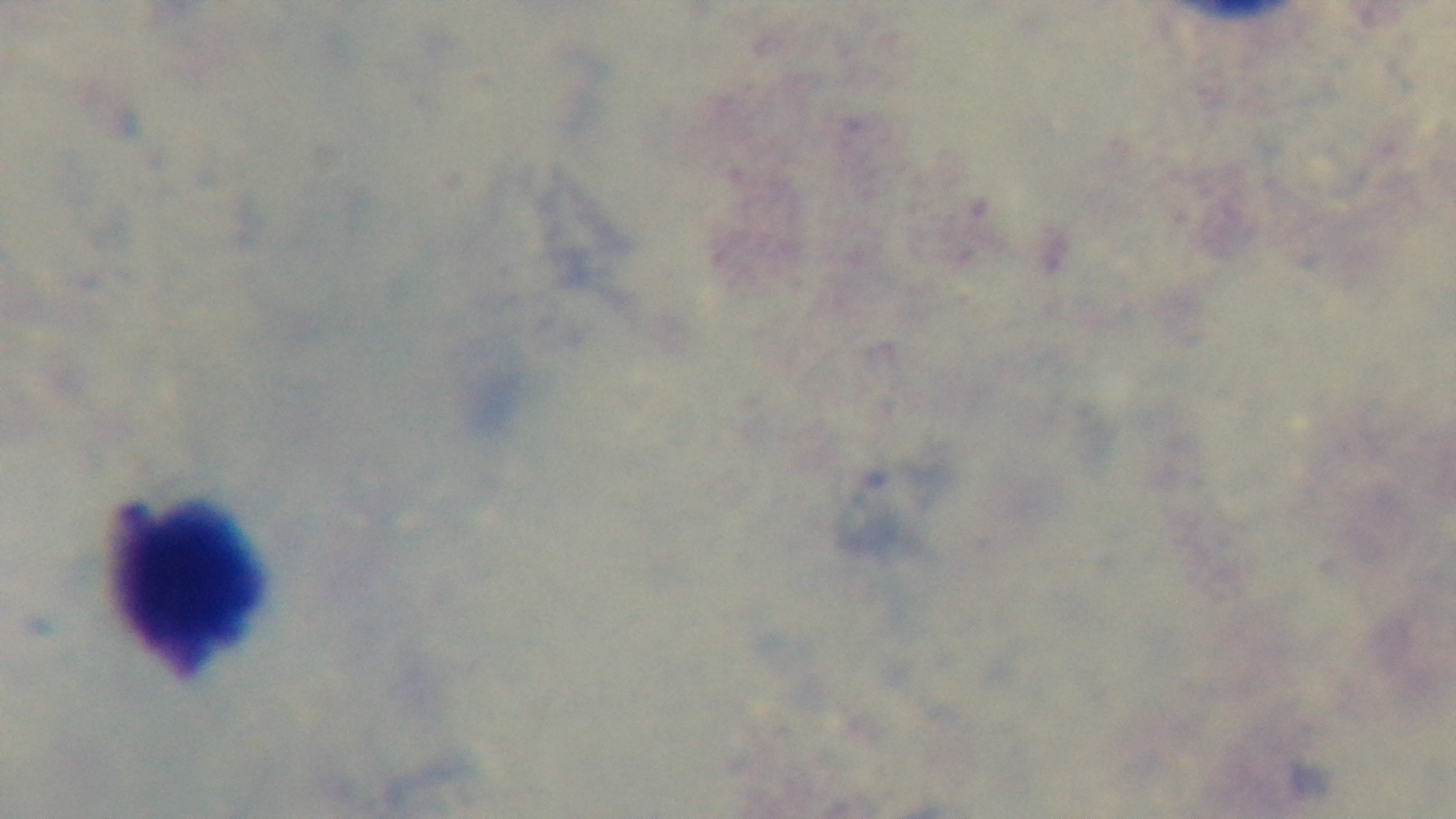
Captured with a mounted 4K digital camera. 100x oil-immersion objective. Single field of view. Preparation: thick smear. Light microscopy. Giemsa stain. Malaria status: uninfected.